Report the malaria status of this cell.
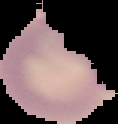
Parasitized.

{
  "preparation": "thin blood smear",
  "image_type": "segmented cell region with the area outside set to black",
  "image_size": "118×124 pixels"
}